Point out each malaria parasite.
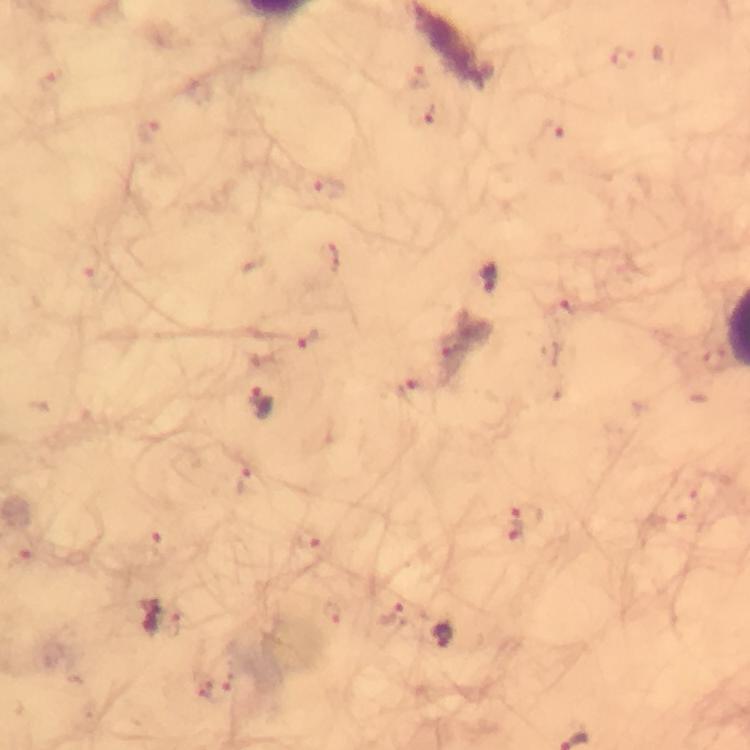

Approximate centers as [x, y] in pixels.
Malaria parasites: [625, 58], [416, 76], [423, 115], [149, 129], [552, 134], [327, 186], [89, 264], [489, 279], [565, 314], [311, 338], [408, 389], [262, 401], [243, 481], [527, 513], [308, 539], [156, 543], [26, 561], [333, 613], [392, 616], [173, 624], [443, 633].

image size = 750×750 pixels
immersion oil = used
capture = smartphone mounted on the microscope
magnification = 100x
preparation = thick smear
context = from a diagnostic examination for malaria
cropped from = a single field of view
stain = Giemsa